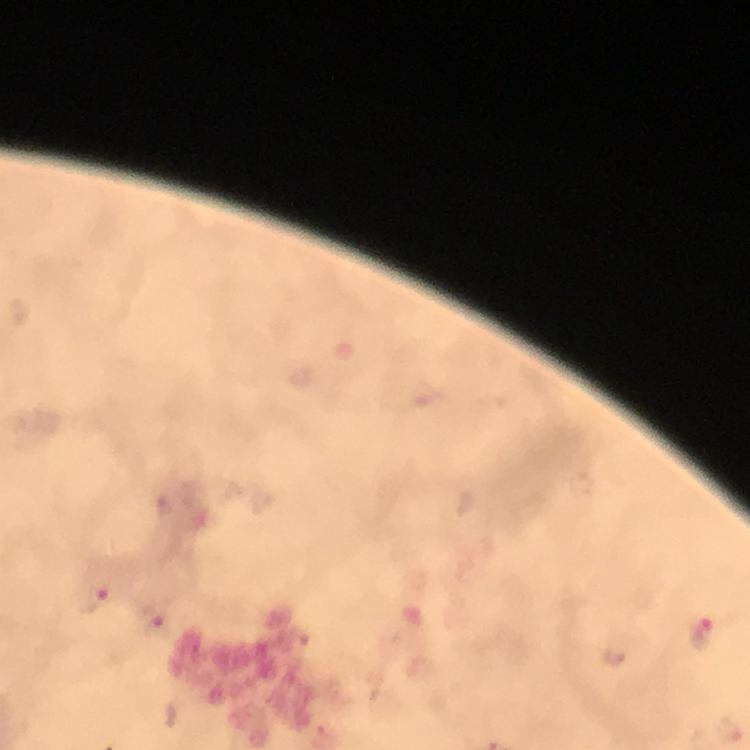 Approximate centers as (x, y) in pixels. Malaria parasite locations: (93, 601), (157, 622), (704, 636), (614, 654). Giemsa stain. Image is 750×750 pixels. Cropped region of a single field of view. At 100x magnification. Smartphone photograph taken through a microscope. Immersion oil was used. From a diagnostic examination for malaria. Thick smear.